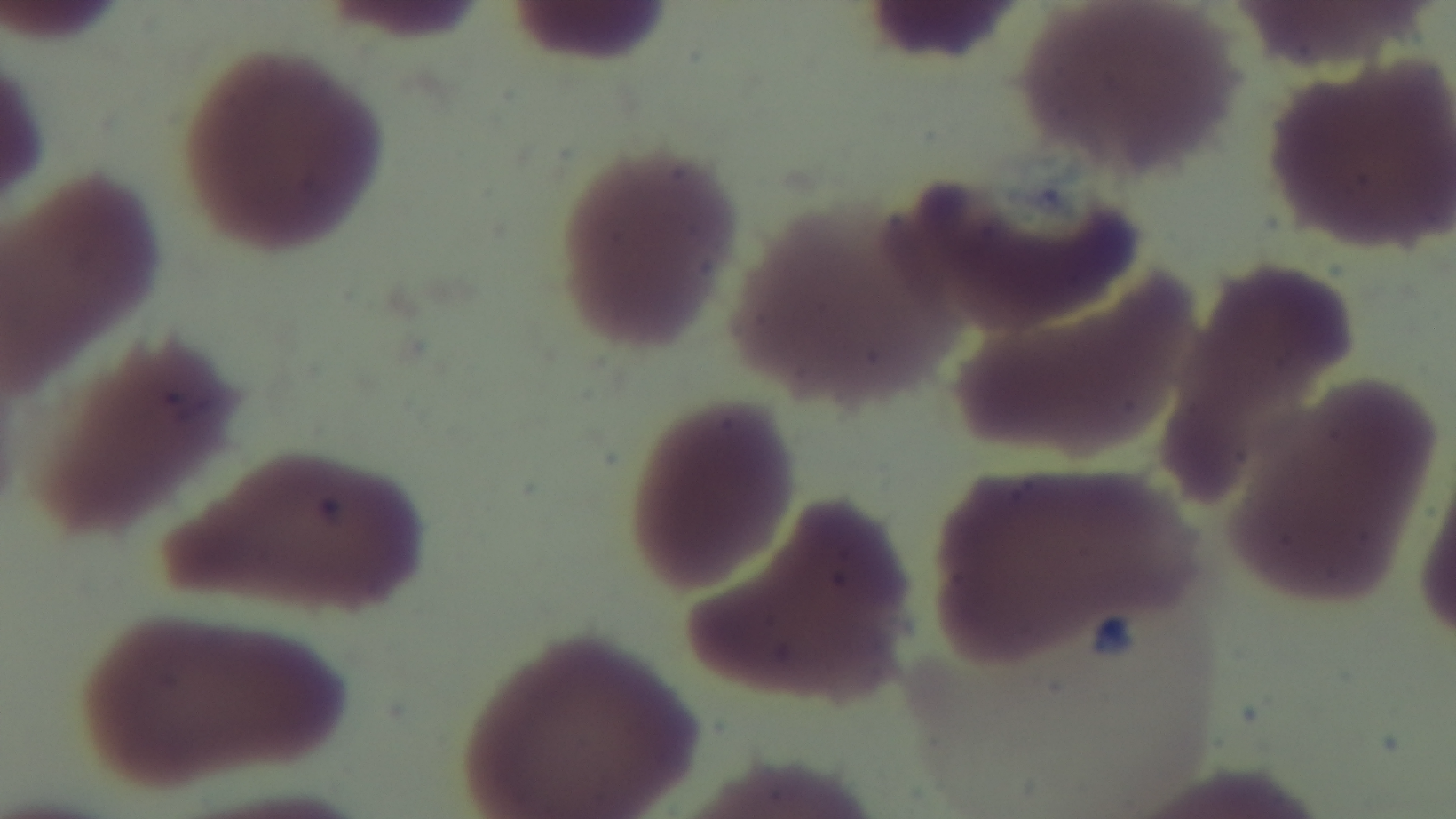
capture = mounted 4K digital camera
objective = 100x oil immersion
field of view = one from the slide
stain = Giemsa
preparation = thin blood film
modality = light microscopy
malaria status = uninfected